Assess this cell for malaria.
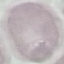
Uninfected.

stain = Giemsa
capture = smartphone through the microscope eyepiece
preparation = thin smear
image type = automatically extracted cell patch, resized to 64 × 64 pixels